Assess the morphology of the red blood cells.
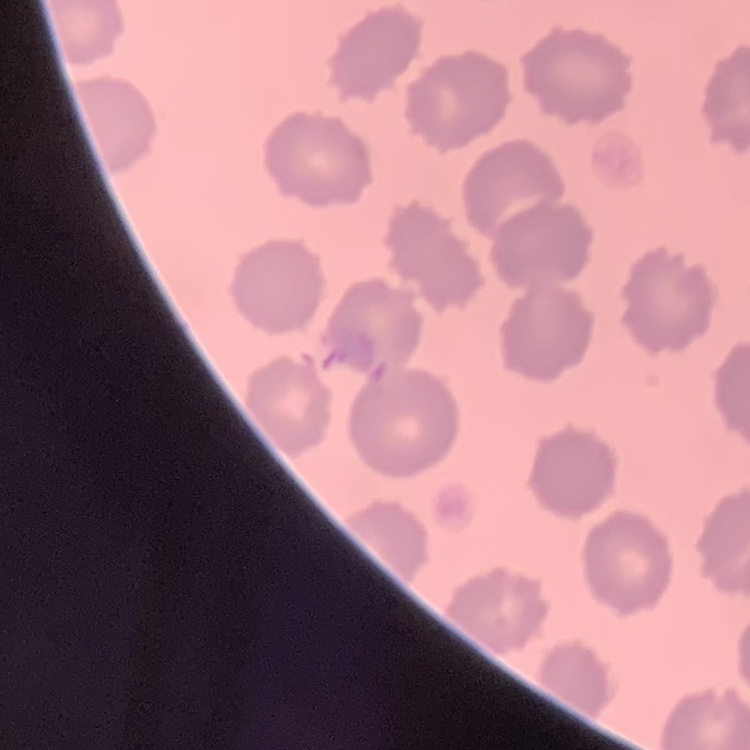

They show no rouleaux formation.

stain = Field's or Giemsa
image type = one tile cut from a larger photomicrograph
preparation = thin blood smear